Give a bounding box for every leukocyte visible.
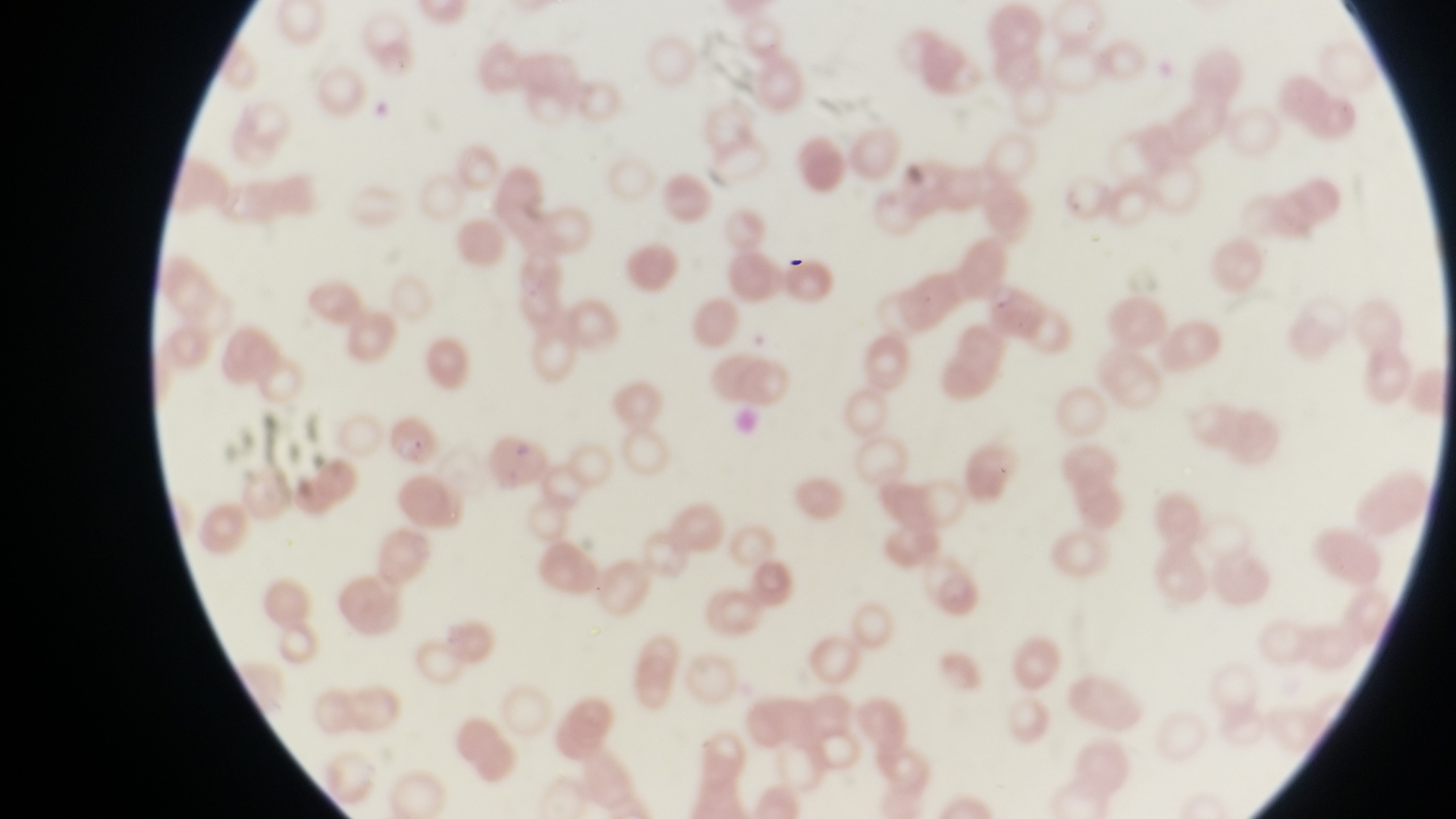

No leukocytes observed.

Approximate bounding boxes as (left, top, right, bottom) in pixels. Artifact (platelet-like body, stain precipitate, or debris) locations: (779, 251, 809, 275). Parasitised red blood cell locations: (386, 407, 441, 465). Magnification of 1000x. Photographed through the eyepiece of an Olympus CX-23 microscope with a smartphone camera. Single field of view. Image is 1456×819 pixels. Thin blood film. Sample from Uganda.